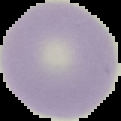
Summary:
  - Image type: cell region segmented out of the field of view; surrounding area masked to black
  - Preparation: thin blood film
  - Image size: 121×121 pixels
  - Result: no malaria parasites seen